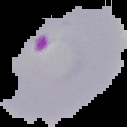

result = malaria parasites detected
preparation = thin blood smear
image size = 127×127 pixels
image type = cell region segmented out of the field of view; surrounding area masked to black